Locate and identify every blood parasite.
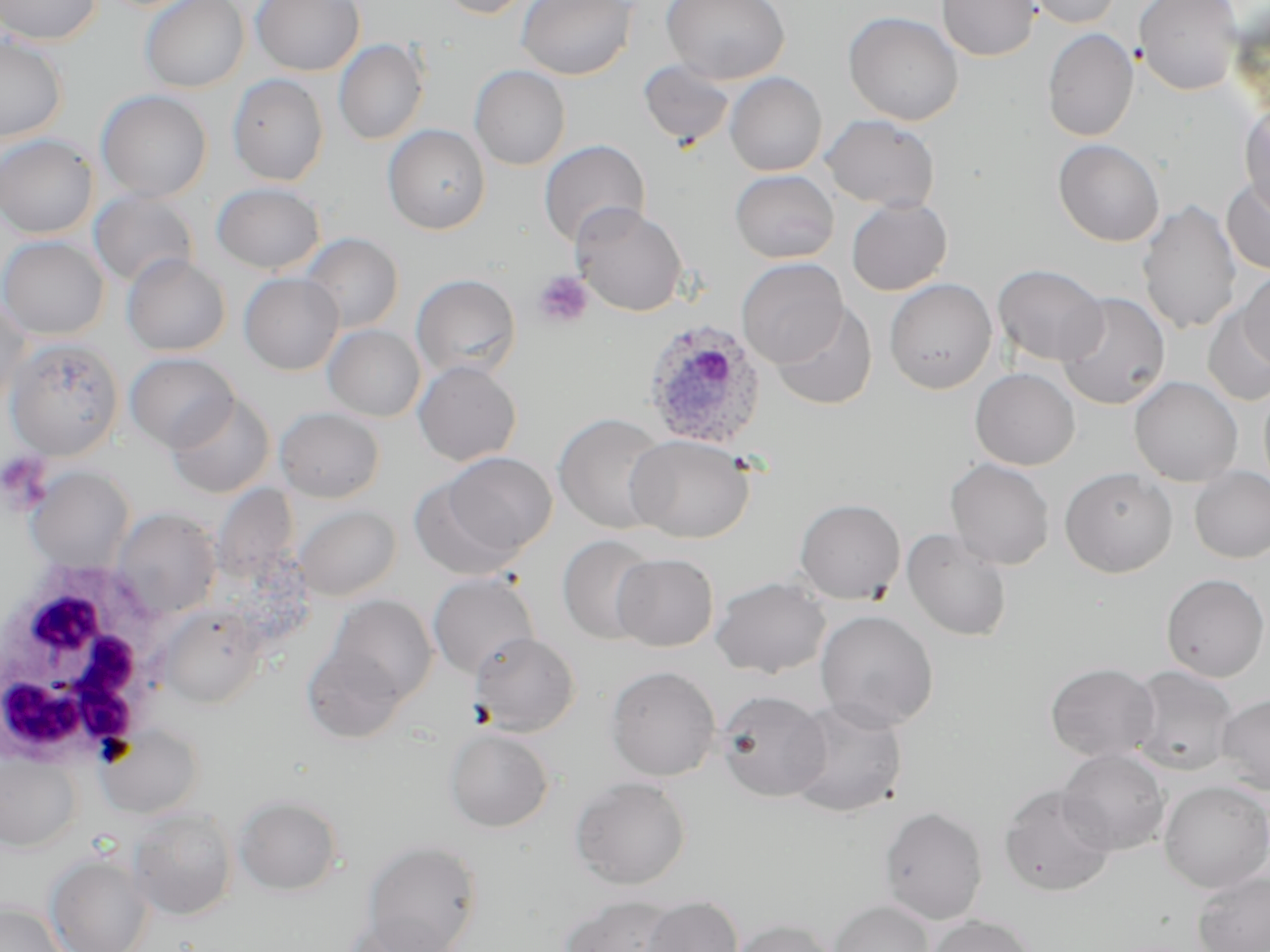

Approximate bounding boxes as (x1, y1, x2, y2) in pixels.
Plasmodium ovale-infected red blood cells: (641, 317, 768, 451).
No Plasmodium falciparum, Plasmodium malariae, Plasmodium vivax, Babesia divergens, or Trypanosoma brucei observed.

Summary:
  - White blood cell locations: (1, 558, 177, 765)
  - Platelet locations: (533, 270, 593, 329), (0, 452, 52, 510)
  - Uninfected red blood cell locations: (1, 0, 103, 45), (140, 0, 249, 93), (250, 0, 365, 76), (435, 0, 535, 19), (516, 0, 637, 80), (661, 0, 790, 84), (937, 0, 1040, 61), (1023, 0, 1122, 28), (1134, 0, 1241, 95), (843, 11, 964, 126), (1042, 28, 1139, 142), (0, 34, 69, 143), (334, 38, 430, 145), (638, 59, 736, 150), (469, 65, 571, 171), (724, 72, 827, 176), (227, 73, 329, 186), (95, 90, 213, 202), (1239, 101, 1270, 220), (821, 114, 941, 212), (383, 124, 490, 234), (0, 134, 99, 238), (1053, 139, 1165, 247), (538, 140, 650, 248), (730, 169, 838, 263), (1221, 174, 1270, 276), (212, 182, 325, 275), (89, 189, 199, 288), (846, 197, 952, 296), (1137, 199, 1243, 336), (572, 202, 688, 316), (299, 233, 404, 333), (0, 235, 109, 339), (121, 254, 230, 356), (736, 258, 848, 368), (992, 263, 1108, 366), (1237, 269, 1270, 371), (239, 273, 344, 375), (411, 274, 521, 381), (884, 278, 997, 394), (1056, 291, 1171, 410), (0, 295, 30, 414), (770, 302, 878, 411), (1202, 308, 1270, 406), (323, 324, 425, 421), (5, 337, 124, 461), (124, 352, 239, 452), (413, 361, 522, 466), (970, 368, 1080, 470), (1129, 376, 1243, 487), (1259, 383, 1270, 495), (166, 393, 275, 499), (275, 407, 385, 503), (553, 413, 671, 533), (627, 434, 754, 544), (435, 451, 556, 564), (945, 458, 1054, 570), (26, 466, 135, 573), (1059, 466, 1177, 577), (1189, 467, 1270, 563), (211, 483, 299, 582), (794, 498, 906, 604), (294, 504, 401, 601), (112, 507, 222, 618), (902, 528, 1012, 641), (557, 534, 659, 645), (612, 552, 719, 651), (427, 573, 540, 679), (1161, 573, 1270, 682), (710, 575, 831, 678), (320, 594, 439, 714), (158, 605, 265, 709), (815, 609, 939, 731), (469, 632, 581, 737), (301, 637, 412, 746), (1045, 662, 1160, 763), (605, 665, 721, 781), (1126, 665, 1239, 776), (715, 689, 831, 802), (1216, 693, 1270, 794), (785, 698, 908, 818), (96, 724, 203, 818), (444, 728, 554, 832), (0, 749, 82, 852), (1056, 749, 1171, 855), (570, 776, 692, 889), (1158, 781, 1270, 893), (999, 784, 1117, 897), (234, 794, 344, 895), (879, 806, 989, 924), (126, 807, 237, 921), (362, 839, 483, 952), (46, 853, 153, 952), (1192, 871, 1270, 952), (558, 895, 685, 952), (641, 896, 743, 952), (0, 900, 67, 952), (829, 900, 934, 952), (926, 914, 1034, 952), (348, 917, 459, 952), (730, 918, 837, 952)
  - Slide-level diagnosis: Plasmodium ovale
  - Stain: May-Grünwald-Giemsa
  - Field of view: one of a larger specimen
  - Modality: optical microscopy
  - Preparation: thin blood film
  - Magnification: 1000x
  - Image size: 1270×952 pixels